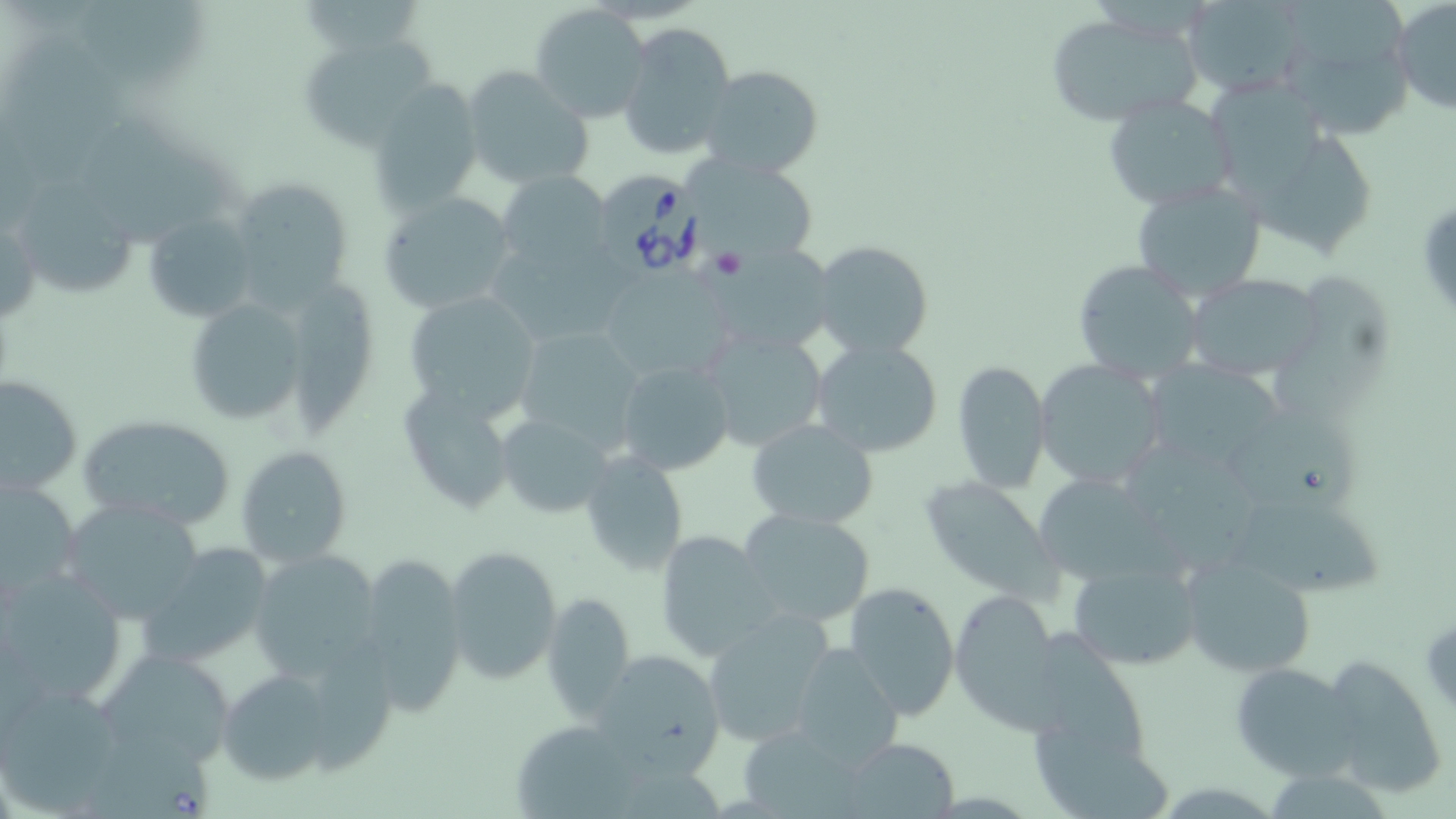 Approximate bounding boxes as (x1,y1)-(x2,y2) corner pairs in pixels. Platelet locations: (717,253)-(751,283). Uninfected red blood cell locations: (1181,0)-(1311,97), (1270,0)-(1416,140), (1392,0)-(1456,116), (74,2)-(217,94), (530,6)-(653,125), (1042,11)-(1204,125), (617,21)-(737,162), (296,34)-(440,152), (461,65)-(594,192), (698,66)-(825,179), (1201,74)-(1333,201), (366,77)-(486,214), (1103,94)-(1237,211), (80,116)-(252,245), (1253,135)-(1385,257), (687,158)-(822,265), (497,169)-(613,271), (225,175)-(358,308), (1130,178)-(1268,303), (24,181)-(151,300), (379,192)-(519,315), (0,209)-(41,329), (143,211)-(258,325), (812,240)-(936,359), (712,246)-(835,356), (1067,257)-(1202,381), (597,271)-(759,377), (1186,273)-(1326,381), (1272,275)-(1405,426), (296,279)-(379,442), (401,288)-(544,421), (179,291)-(315,430), (511,324)-(647,451), (698,327)-(829,453), (809,339)-(946,460), (616,360)-(737,478), (951,360)-(1051,494), (1034,360)-(1167,492), (1149,362)-(1294,469), (2,373)-(85,496), (396,381)-(520,516), (74,411)-(239,531), (496,413)-(616,517), (1232,414)-(1381,534), (745,418)-(880,529), (236,445)-(354,567), (579,454)-(690,578), (918,473)-(1060,599), (1040,477)-(1193,580), (1,478)-(83,599), (62,499)-(206,626), (1229,501)-(1388,605), (737,506)-(875,629), (654,530)-(778,661), (139,544)-(274,670), (442,544)-(562,686), (249,549)-(381,677), (1179,552)-(1319,678), (353,556)-(467,716), (1066,559)-(1203,670), (2,568)-(129,704), (844,580)-(960,722), (948,589)-(1060,726), (543,590)-(635,723), (700,611)-(836,748), (1040,625)-(1152,775), (786,643)-(905,766), (95,646)-(237,772), (590,647)-(728,774), (1317,653)-(1448,799), (1228,661)-(1357,779), (217,667)-(338,785), (3,682)-(126,808), (841,736)-(961,817). Babesia divergens-infected red blood cell locations: (597,170)-(717,280). Slide-level diagnosis: Babesia divergens. 1000x magnification. Optical microscopy. Image is 1456×819 pixels. One field of a larger specimen. Thin blood smear. May-Grünwald-Giemsa stain.